Locate every Plasmodium ovale-infected red blood cell.
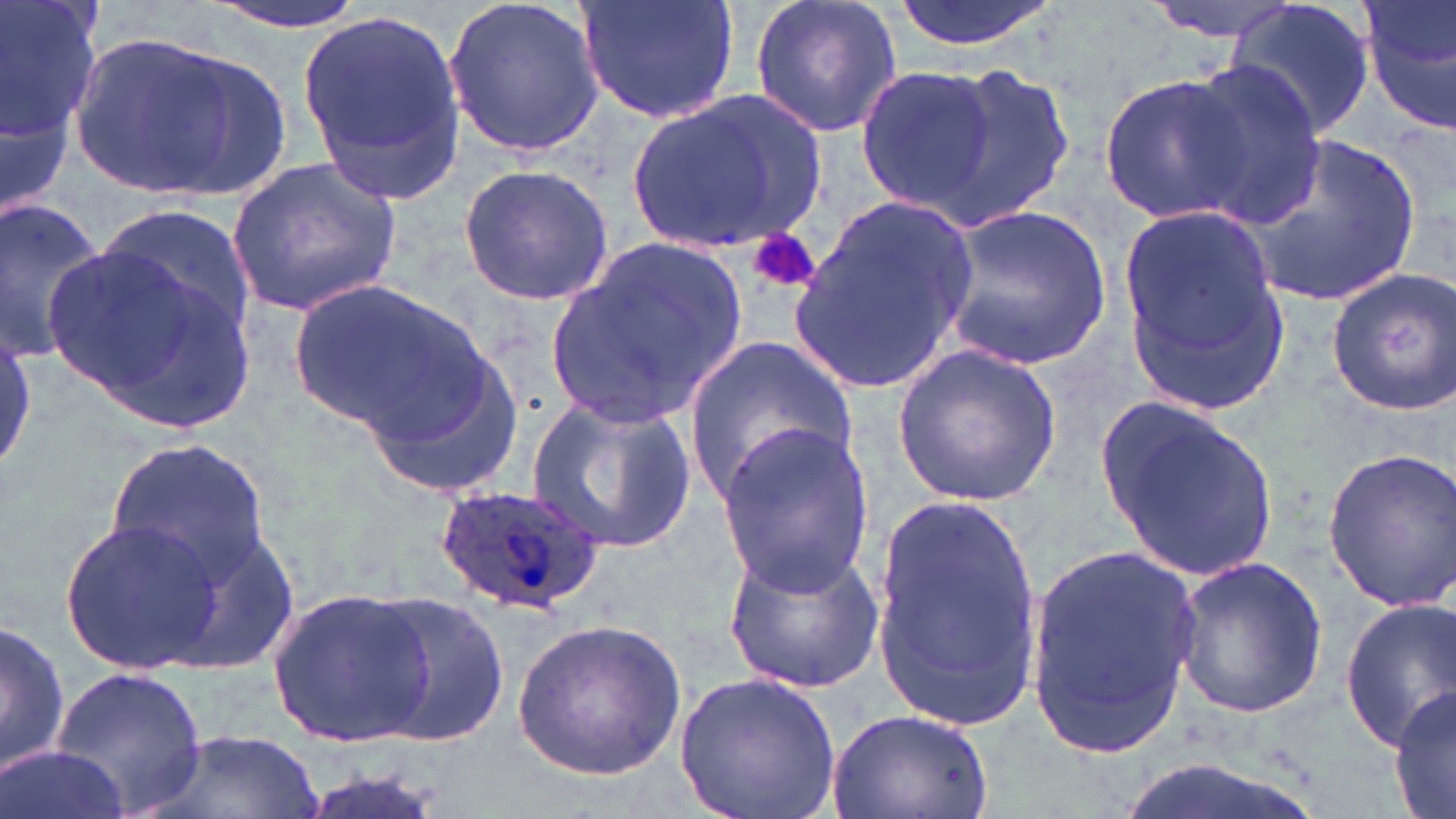

Approximate bounding boxes as (x1,y1)-(x2,y2) corner pairs in pixels.
Plasmodium ovale-infected red blood cells: (435,483)-(608,614).

Uninfected red blood cell locations: (0,0)-(100,204), (195,0)-(375,34), (444,0)-(604,157), (578,0)-(739,126), (748,0)-(903,140), (891,0)-(1058,54), (1145,0)-(1302,41), (1228,0)-(1376,140), (1358,0)-(1456,133), (297,10)-(466,201), (65,29)-(259,200), (927,60)-(1076,229), (1174,63)-(1324,228), (853,65)-(1003,217), (1100,71)-(1251,224), (626,88)-(829,262), (1234,132)-(1427,307), (227,155)-(406,315), (456,165)-(615,306), (787,196)-(980,391), (0,200)-(108,363), (938,204)-(1111,373), (1119,204)-(1288,407), (94,205)-(258,355), (42,226)-(265,437), (544,236)-(752,425), (1325,268)-(1455,415), (284,279)-(488,436), (0,326)-(36,475), (355,337)-(526,497), (682,337)-(856,504), (891,344)-(1062,506), (528,394)-(695,554), (1100,400)-(1279,584), (711,424)-(880,593), (105,435)-(275,579), (1321,447)-(1456,611), (870,493)-(1048,733), (58,516)-(228,675), (1027,541)-(1207,757), (722,542)-(885,694), (1173,556)-(1327,718), (266,584)-(437,750), (367,593)-(510,747), (1341,597)-(1456,750), (513,617)-(685,778), (1,619)-(70,776), (48,663)-(208,816), (674,670)-(846,819), (1388,679)-(1456,819), (821,708)-(997,819), (141,729)-(326,819), (5,747)-(122,819), (297,765)-(452,819). Platelet locations: (751,229)-(819,292). Slide-level diagnosis: Plasmodium ovale. Single field of view. 1000x magnification. Optical microscopy. May-Grünwald-Giemsa-stained preparation. Thin blood film. Image is 1456×819 pixels.